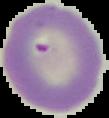

result: no Plasmodium parasites detected
preparation: thin blood smear
image_type: segmented cell region on a black background
image_size: 109×118 pixels